Describe the morphology of the erythrocytes.
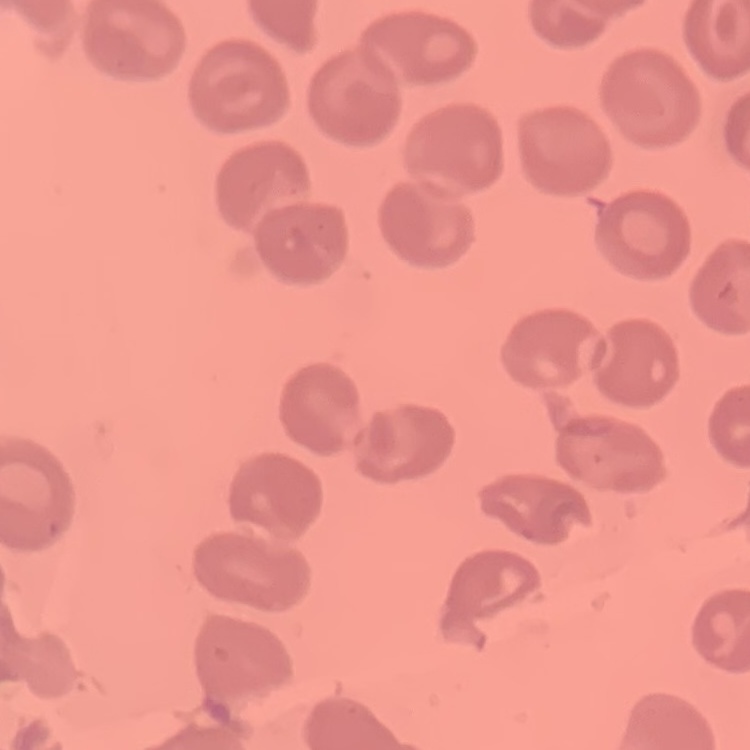

They show no rouleaux formation.

{
  "preparation": "thin peripheral smear",
  "image_type": "square crop of a larger photomicrograph",
  "stain": "Field's or Giemsa"
}